Report the malaria status of this cell.
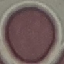

Uninfected.

{
  "image_type": "cell patch, automatically extracted from a larger field of view and resized to 64 × 64 pixels",
  "preparation": "thin blood smear",
  "capture": "smartphone through the microscope eyepiece",
  "stain": "Giemsa"
}